Report the malaria status of this cell.
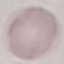
It is uninfected.

image type = automatically extracted cell patch, resized to 64 × 64 pixels
stain = Giemsa
preparation = thin blood smear
capture = smartphone camera at the microscope eyepiece